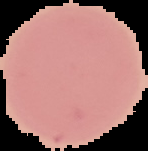
image size = 148×151 pixels
malaria status = uninfected
image type = cell region segmented out of the field of view; surrounding area masked to black
preparation = thin blood smear